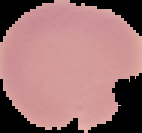

From a thin blood smear. Image is 142×133 pixels. Segmented cell region on a black background. Malaria status: uninfected.